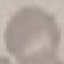
Summary:
  - Result: negative for malaria parasites
  - Image type: automatically extracted cell patch, resized to 64 × 64 pixels
  - Preparation: thin smear
  - Capture: smartphone camera at the microscope eyepiece
  - Stain: Giemsa